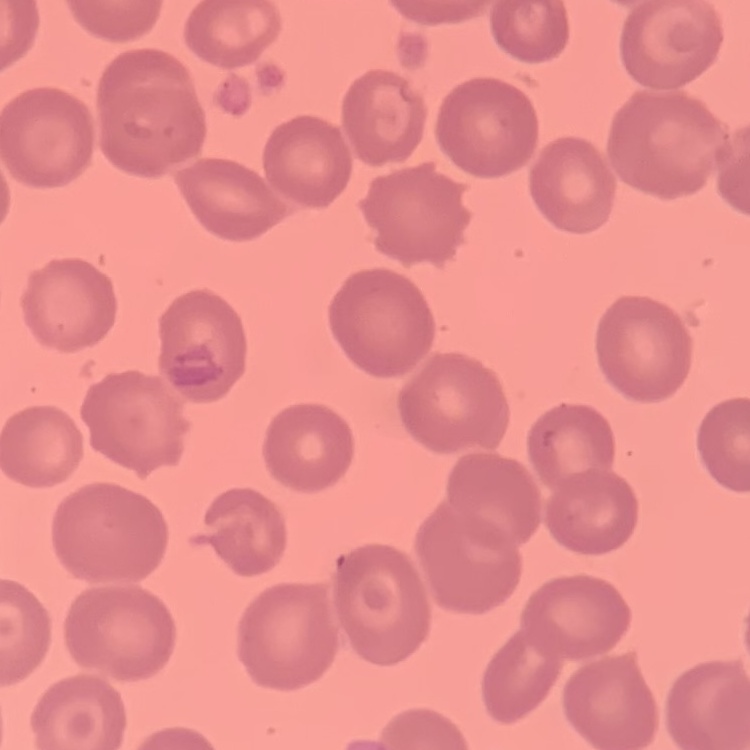
red_blood_cell_morphology: no rouleaux formation
image_type: square crop of a larger photomicrograph
preparation: thin blood smear
stain: Field's or Giemsa